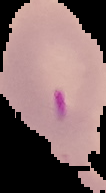

Image is 106×193 pixels. Result: negative for Plasmodium parasites. Cell region segmented out of the field of view; the surrounding area is masked to black. From a thin blood smear.